Report the malaria status of this cell.
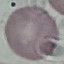

Uninfected.

Thin blood film. Giemsa-stained preparation. Automatically extracted cell patch, resized to 64 × 64 pixels. Acquired by smartphone through the microscope eyepiece.